Report the malaria status of this cell.
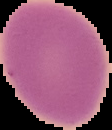

It is uninfected.

Image is 112×130 pixels. From a thin blood smear. The area outside the segmented cell region is set to black.